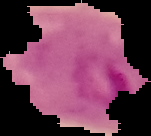
Image is 151×136 pixels. From a thin blood film. Cell region segmented out of the field of view; the surrounding area is masked to black. Result: malaria parasites detected.